Give the position of every malaria parasite.
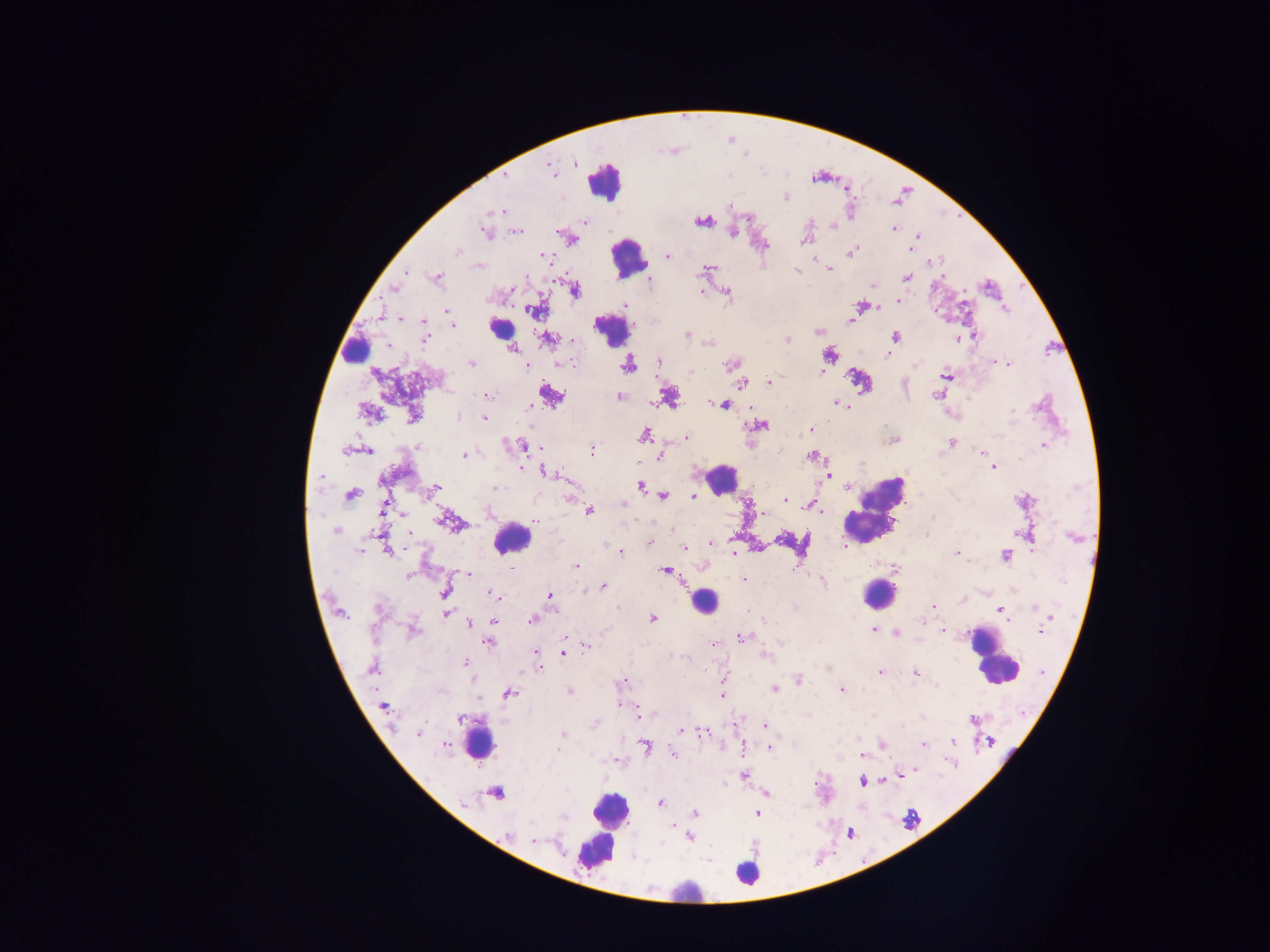
Approximate centers as [x, y] in pixels.
Malaria parasites: [575, 163], [549, 168], [506, 176], [786, 197], [501, 210], [702, 222], [585, 223], [834, 226], [894, 229], [609, 230], [485, 231], [517, 231], [733, 233], [918, 235], [805, 239], [910, 249], [455, 253], [851, 253], [544, 255], [668, 256], [933, 262], [708, 269], [829, 269], [797, 270], [407, 272], [906, 278], [437, 279], [649, 281], [395, 289], [511, 289], [575, 291], [701, 291], [727, 293], [899, 302], [625, 304], [862, 306], [1005, 309], [532, 310], [446, 311], [400, 318], [850, 320], [424, 321], [451, 321], [453, 326], [818, 332], [687, 335], [974, 335], [895, 336], [424, 339], [547, 339], [958, 339], [572, 340], [788, 340], [512, 348], [827, 354], [887, 354], [659, 362], [471, 363], [999, 363], [571, 364], [731, 364], [1008, 364], [630, 365], [527, 367], [821, 371], [690, 372], [947, 376], [769, 382], [741, 384], [551, 394], [487, 395], [936, 395], [620, 397], [837, 403], [715, 404], [724, 405], [530, 406], [1012, 410], [369, 412], [414, 417], [457, 417], [484, 417], [760, 425], [811, 429], [644, 434], [686, 437], [894, 441], [951, 442], [1043, 445], [525, 446], [418, 447], [345, 450], [367, 450], [591, 450], [981, 452], [464, 455], [660, 456], [812, 457], [521, 467], [994, 467], [545, 472], [828, 475], [322, 476], [640, 486], [436, 487], [847, 487], [497, 488], [350, 494], [664, 496], [694, 497], [785, 500], [624, 505], [384, 506], [807, 506], [589, 511], [821, 512], [763, 513], [401, 514], [934, 518], [537, 520], [443, 521], [672, 529], [335, 531], [409, 533], [926, 535], [1073, 537], [650, 543], [711, 543], [684, 548], [387, 550], [1032, 550], [360, 552], [620, 552], [734, 553], [957, 553], [1005, 555], [576, 565], [511, 569], [665, 571], [467, 573], [408, 576], [744, 579], [822, 582], [602, 586], [445, 591], [585, 591], [492, 594], [550, 596], [933, 606], [617, 608], [1036, 608], [1000, 609], [446, 612], [1051, 617], [652, 619], [532, 620], [494, 621], [469, 623], [874, 630], [414, 631], [1040, 631], [943, 632], [895, 634], [742, 637], [489, 642], [714, 644], [585, 646], [535, 652], [563, 652], [765, 656], [683, 657], [465, 662], [372, 668], [539, 669], [879, 672], [917, 674], [624, 680], [798, 681], [724, 682], [774, 689], [842, 690], [569, 691], [507, 694], [723, 695], [383, 707], [654, 714], [461, 719], [972, 720], [765, 726], [681, 730], [703, 732], [418, 733], [562, 734], [989, 741], [953, 742], [446, 744], [883, 745], [923, 745], [645, 746], [770, 748], [558, 750], [674, 753], [860, 755], [916, 769], [902, 774], [744, 775], [862, 781], [883, 782], [496, 793], [766, 793], [660, 803], [695, 813], [757, 813], [563, 818], [508, 834], [689, 838], [534, 841].

Summary:
  - Leukocyte locations: [604, 180], [628, 259], [501, 328], [611, 329], [354, 348], [721, 479], [873, 511], [511, 538], [877, 594], [705, 601], [994, 662], [479, 745], [608, 811], [602, 834], [597, 851], [750, 873], [683, 893]
  - Preparation: thick blood film
  - Image size: 1270×952 pixels
  - Field of view: single
  - Country: Ghana
  - Capture: mobile-phone photograph through a microscope